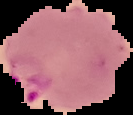
result: Plasmodium parasites detected
preparation: thin blood film
image_size: 133×115 pixels
image_type: segmented cell region with the area outside set to black